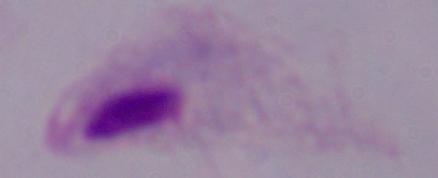

Micrograph. 1000x magnification. A trichomonad is shown.